Describe the morphology of the erythrocytes.
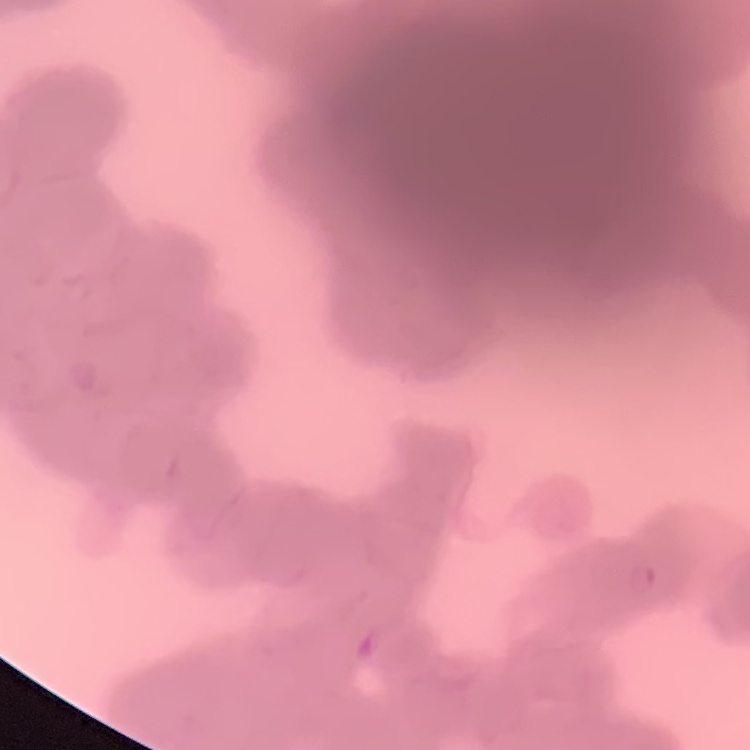
They show rouleaux formation.

{
  "preparation": "thin peripheral smear",
  "image_type": "square crop of a larger photomicrograph",
  "stain": "Field's or Giemsa"
}